Assess the morphology of the red blood cells.
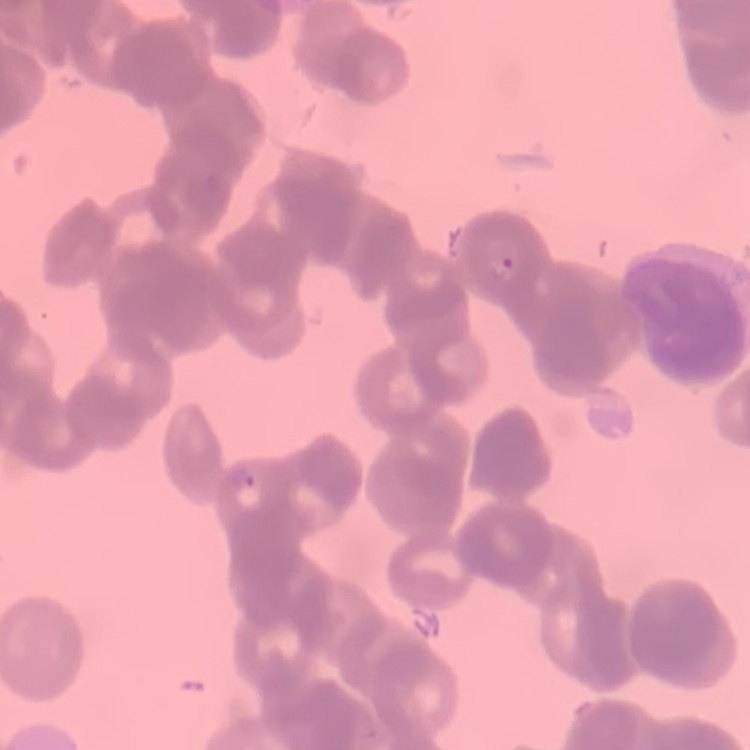
Rouleaux formation.

stain = Field's or Giemsa
image type = square crop of a larger photomicrograph
preparation = thin blood film